Locate and identify every blood parasite.
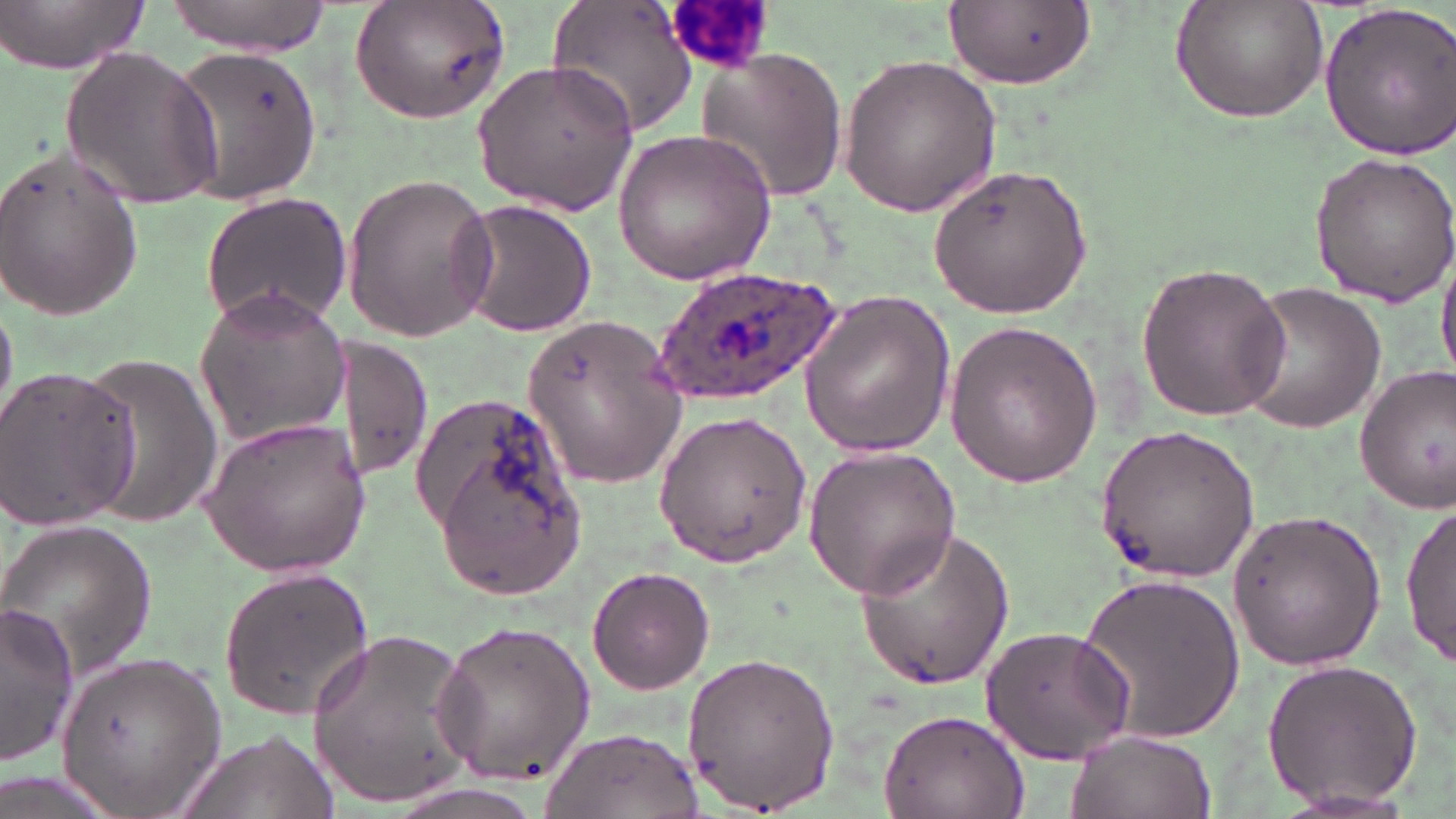
Approximate bounding boxes as (x1, y1, x2, y2) in pixels.
Plasmodium ovale-infected red blood cells: (652, 267, 846, 407).
No Plasmodium falciparum, Plasmodium malariae, Plasmodium vivax, Babesia divergens, or Trypanosoma brucei observed.

Summary:
  - Uninfected red blood cell locations: (1, 0, 151, 74), (163, 0, 335, 56), (350, 0, 514, 125), (546, 0, 700, 142), (1169, 0, 1330, 123), (941, 2, 1095, 92), (1319, 2, 1456, 158), (165, 42, 325, 210), (698, 44, 850, 201), (58, 46, 224, 209), (838, 53, 1002, 218), (469, 59, 639, 215), (611, 128, 776, 284), (0, 140, 145, 326), (1308, 150, 1456, 307), (924, 162, 1094, 317), (338, 171, 497, 342), (201, 193, 351, 328), (454, 198, 597, 339), (1435, 245, 1456, 386), (1134, 260, 1290, 421), (1234, 281, 1388, 436), (798, 284, 956, 462), (192, 287, 352, 447), (523, 312, 688, 490), (944, 316, 1105, 488), (333, 336, 434, 484), (77, 352, 223, 528), (0, 362, 140, 533), (1354, 363, 1456, 512), (420, 401, 588, 603), (653, 410, 812, 566), (198, 415, 370, 578), (1093, 421, 1260, 586), (802, 444, 962, 599), (1400, 502, 1455, 667), (1228, 506, 1389, 671), (0, 519, 158, 682), (856, 527, 1015, 690), (217, 565, 375, 719), (586, 566, 715, 695), (1074, 572, 1248, 744), (1, 606, 80, 762), (431, 614, 597, 790), (307, 625, 480, 809), (981, 625, 1136, 763), (677, 648, 844, 814), (53, 649, 224, 815), (1259, 656, 1425, 811), (882, 706, 1028, 818), (541, 728, 702, 819), (1065, 728, 1216, 819), (175, 729, 336, 819), (0, 770, 122, 819), (1264, 787, 1427, 818)
  - Slide-level diagnosis: Plasmodium ovale
  - Field of view: single
  - Preparation: thin blood smear
  - Magnification: 1000x
  - Stain: May-Grünwald-Giemsa
  - Image size: 1456×819 pixels
  - Modality: light microscopy